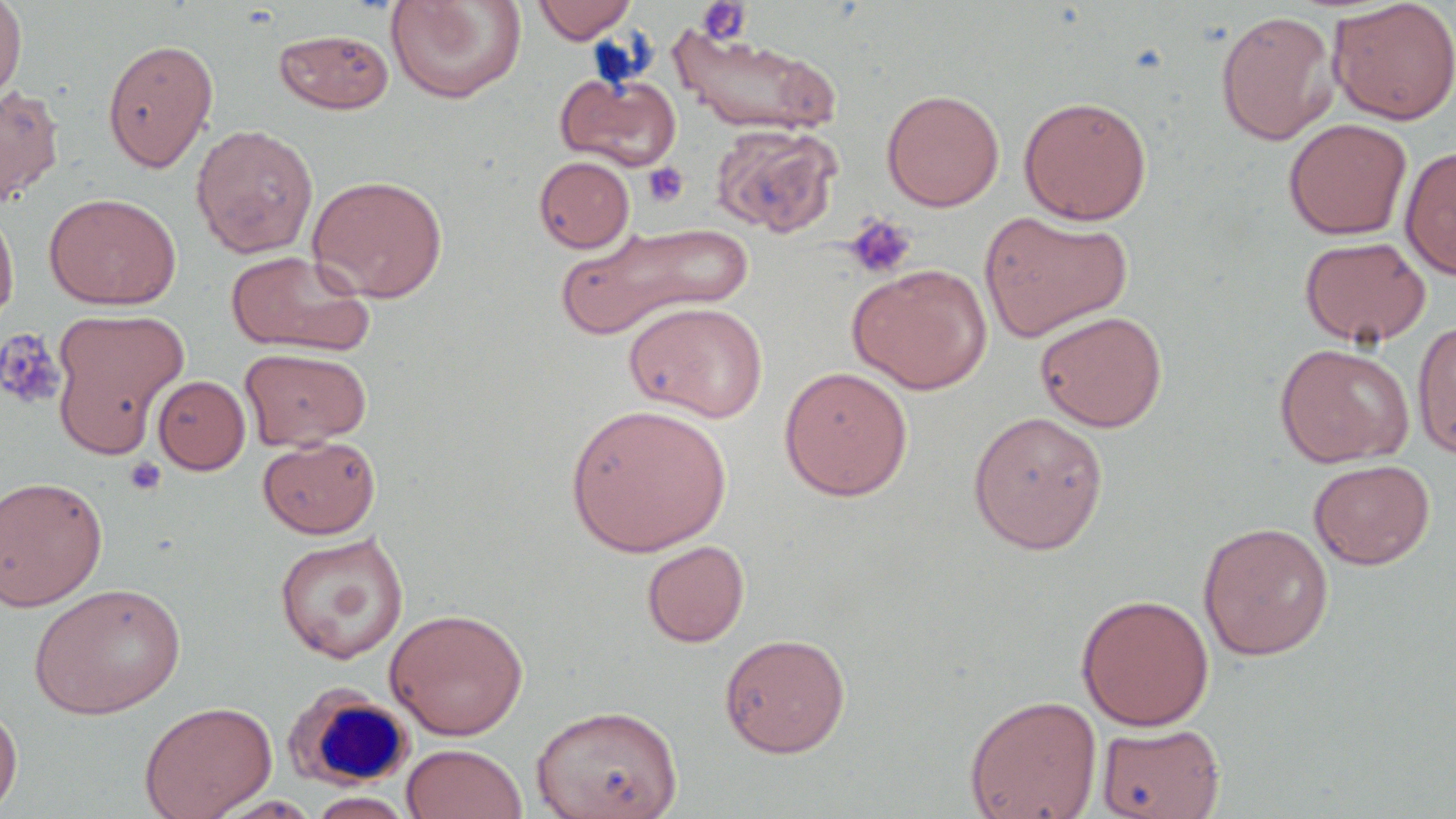
{
  "slide_level_diagnosis": "no evidence of blood parasites",
  "uninfected_red_blood_cell_locations": "approximate bounding boxes as (x1,y1)-(x2,y2) corner pairs in pixels: (0,0)-(27,102), (384,0)-(527,104), (531,0)-(638,43), (1328,0)-(1456,125), (1215,10)-(1339,146), (668,27)-(842,138), (273,28)-(395,114), (102,37)-(218,173), (557,71)-(683,171), (0,84)-(64,207), (882,89)-(1004,211), (1018,95)-(1152,225), (1283,118)-(1412,240), (190,123)-(319,258), (711,124)-(842,238), (1399,145)-(1456,281), (534,156)-(635,253), (308,174)-(448,303), (43,192)-(181,310), (0,201)-(19,333), (980,210)-(1133,342), (556,220)-(753,340), (1299,235)-(1431,348), (225,250)-(376,357), (848,263)-(992,394), (624,301)-(768,423), (51,308)-(188,449), (1034,310)-(1168,432), (1412,320)-(1456,458), (1274,342)-(1414,467), (240,347)-(372,450), (778,365)-(914,501), (153,375)-(250,474), (565,403)-(732,557), (968,409)-(1109,554), (258,435)-(381,539), (1308,459)-(1435,569), (1,475)-(108,610), (1197,521)-(1334,660), (274,532)-(409,664), (641,539)-(750,647), (28,582)-(186,719), (1076,593)-(1214,730), (384,607)-(529,740), (718,632)-(851,758), (964,693)-(1102,819), (0,698)-(23,816), (138,699)-(277,819), (531,704)-(682,819), (1096,722)-(1224,819), (401,743)-(528,819), (306,791)-(417,819)",
  "stain": "May-Grünwald-Giemsa",
  "preparation": "thin blood smear",
  "magnification": "1000x",
  "field_of_view": "one of a larger specimen",
  "white_blood_cell_locations": "approximate bounding boxes as (x1,y1)-(x2,y2) corner pairs in pixels: (284,684)-(413,791)",
  "image_size": "1456×819 pixels",
  "platelet_locations": "approximate bounding boxes as (x1,y1)-(x2,y2) corner pairs in pixels: (696,1)-(752,45), (642,162)-(689,207), (843,214)-(917,280), (0,329)-(67,411), (124,456)-(167,496)",
  "modality": "optical microscopy"
}